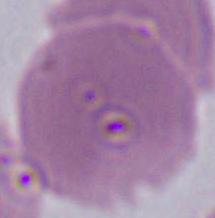

{
  "magnification": "1000x",
  "identification": "red blood cell",
  "modality": "photomicrograph"
}